Classify this cell by malaria status.
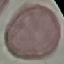

It is uninfected.

Summary:
  - Preparation: thin blood smear
  - Capture: smartphone through the microscope eyepiece
  - Image type: cell patch, automatically extracted from a larger field of view and resized to 64 × 64 pixels
  - Stain: Giemsa